Classify this cell by malaria status.
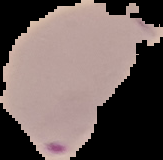

Parasitized.

{
  "image_size": "163×160 pixels",
  "image_type": "cell region segmented out of the field of view; surrounding area masked to black",
  "preparation": "thin blood film"
}